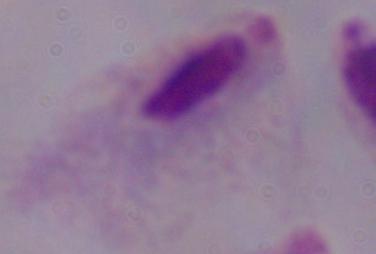
{
  "magnification": "1000x",
  "modality": "micrograph",
  "identification": "trichomonad"
}